Give the extent of all Plasmodium falciparum-infected red blood cells.
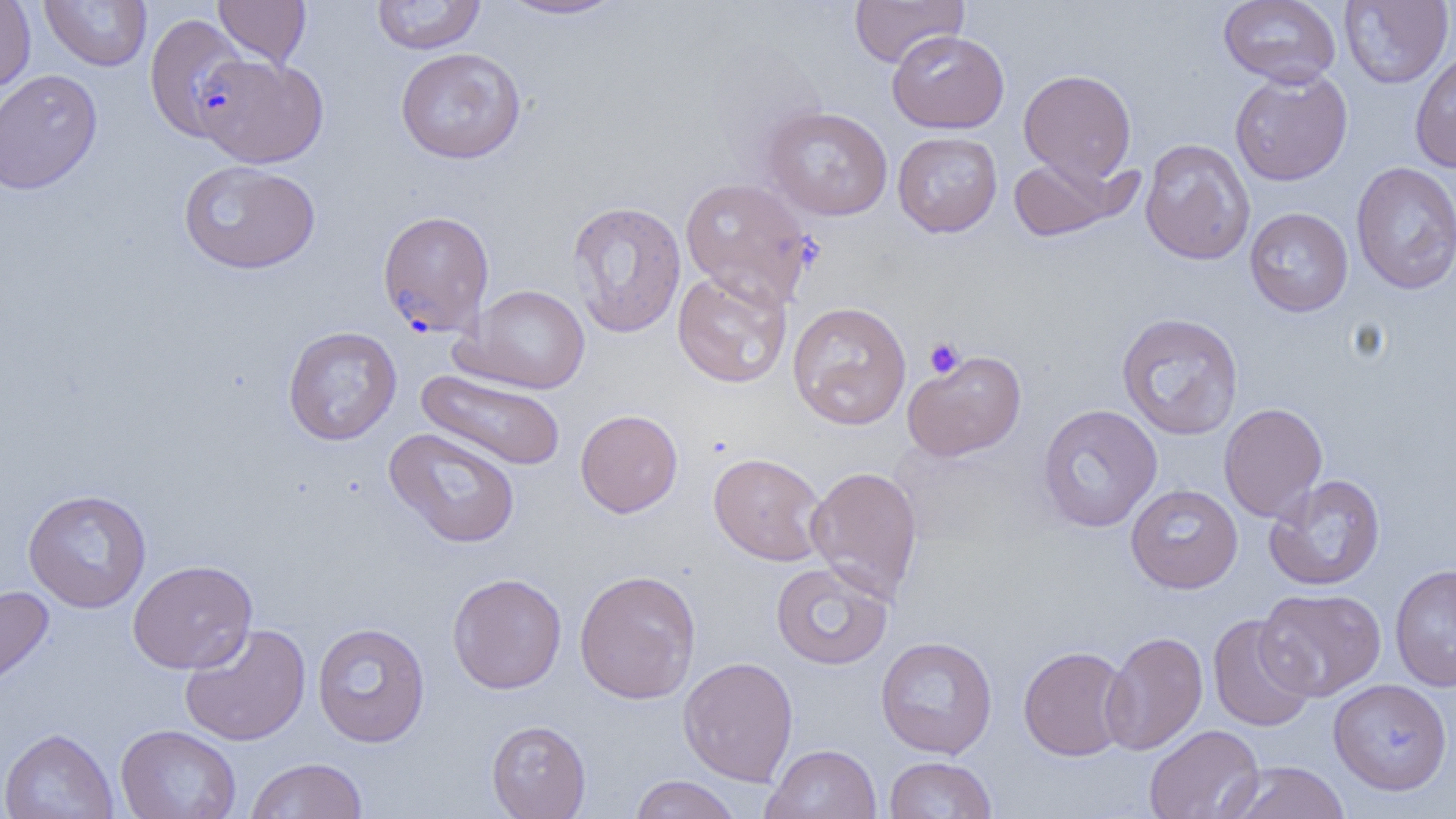

Approximate bounding boxes as (x1,y1)-(x2,y2) corner pairs in pixels.
Plasmodium falciparum-infected red blood cells (subset): (377,210)-(495,337).

Uninfected red blood cell locations (subset): (0,0)-(36,96), (40,0)-(152,72), (213,0)-(311,68), (371,0)-(486,55), (495,0)-(628,20), (849,0)-(968,68), (1218,0)-(1341,87), (1339,0)-(1454,88), (887,29)-(1009,133), (395,47)-(526,164), (1409,50)-(1456,173), (195,53)-(328,167), (1229,67)-(1353,186), (0,68)-(103,195), (1019,69)-(1136,184), (762,106)-(893,221), (892,131)-(1002,237), (1140,139)-(1255,265), (1007,154)-(1131,242), (178,160)-(321,274), (1351,162)-(1456,293), (679,177)-(814,308), (1243,197)-(1456,305), (566,200)-(687,338), (1244,207)-(1353,317), (673,269)-(792,388), (460,284)-(592,394), (787,301)-(912,430), (1116,312)-(1244,440), (283,325)-(402,445), (902,350)-(1027,461), (415,368)-(567,471), (1218,403)-(1328,522), (1037,404)-(1162,532), (575,409)-(683,517), (384,428)-(521,548), (708,452)-(828,566), (806,465)-(923,603), (1264,474)-(1386,591), (1126,484)-(1243,593), (22,488)-(152,613), (128,559)-(257,674), (770,562)-(893,670), (1390,563)-(1456,691), (574,569)-(701,704), (447,572)-(566,694), (0,585)-(55,693), (1257,588)-(1386,700), (1207,613)-(1316,732), (312,622)-(431,747), (179,623)-(311,746), (1100,631)-(1208,756), (875,636)-(998,758), (1018,645)-(1132,761), (678,656)-(798,786), (1328,678)-(1453,796), (487,719)-(591,819), (115,724)-(241,819), (1144,724)-(1264,819), (0,728)-(119,819), (762,744)-(881,819), (884,756)-(997,818), (246,757)-(368,819), (1222,761)-(1351,819), (628,775)-(742,819). Platelet locations: (923,337)-(964,379). Slide-level diagnosis: Plasmodium falciparum. Image is 1456×819 pixels. One field of a larger specimen. Light microscopy. Thin blood film. Captured at 1000x magnification.